Classify this cell by malaria status.
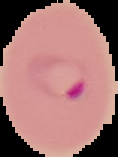

Parasitized.

image type = segmented cell region with the area outside set to black
image size = 118×157 pixels
preparation = thin blood film